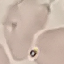 Result: no malaria parasites detected. Thin smear of blood. Cell patch, automatically extracted from a larger field of view and resized to 64 × 64 pixels. Giemsa stain. Photographed with a smartphone camera at the microscope eyepiece.